State which cell type is depicted.
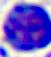

This is a leukocyte.

Photomicrograph. 400x magnification.